Assess this cell for malaria.
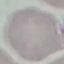

It is uninfected.

Summary:
  - Image type: automatically extracted cell patch, resized to 64 × 64 pixels
  - Stain: Giemsa
  - Preparation: thin blood smear
  - Capture: smartphone through the microscope eyepiece